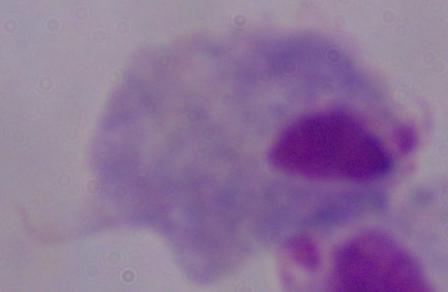
1000x magnification. Micrograph. A trichomonad is shown.